Assess this cell for malaria.
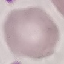

It is uninfected.

Automatically extracted cell patch, resized to 64 × 64 pixels. Acquired by smartphone through the microscope eyepiece. Giemsa stain. Thin blood film.